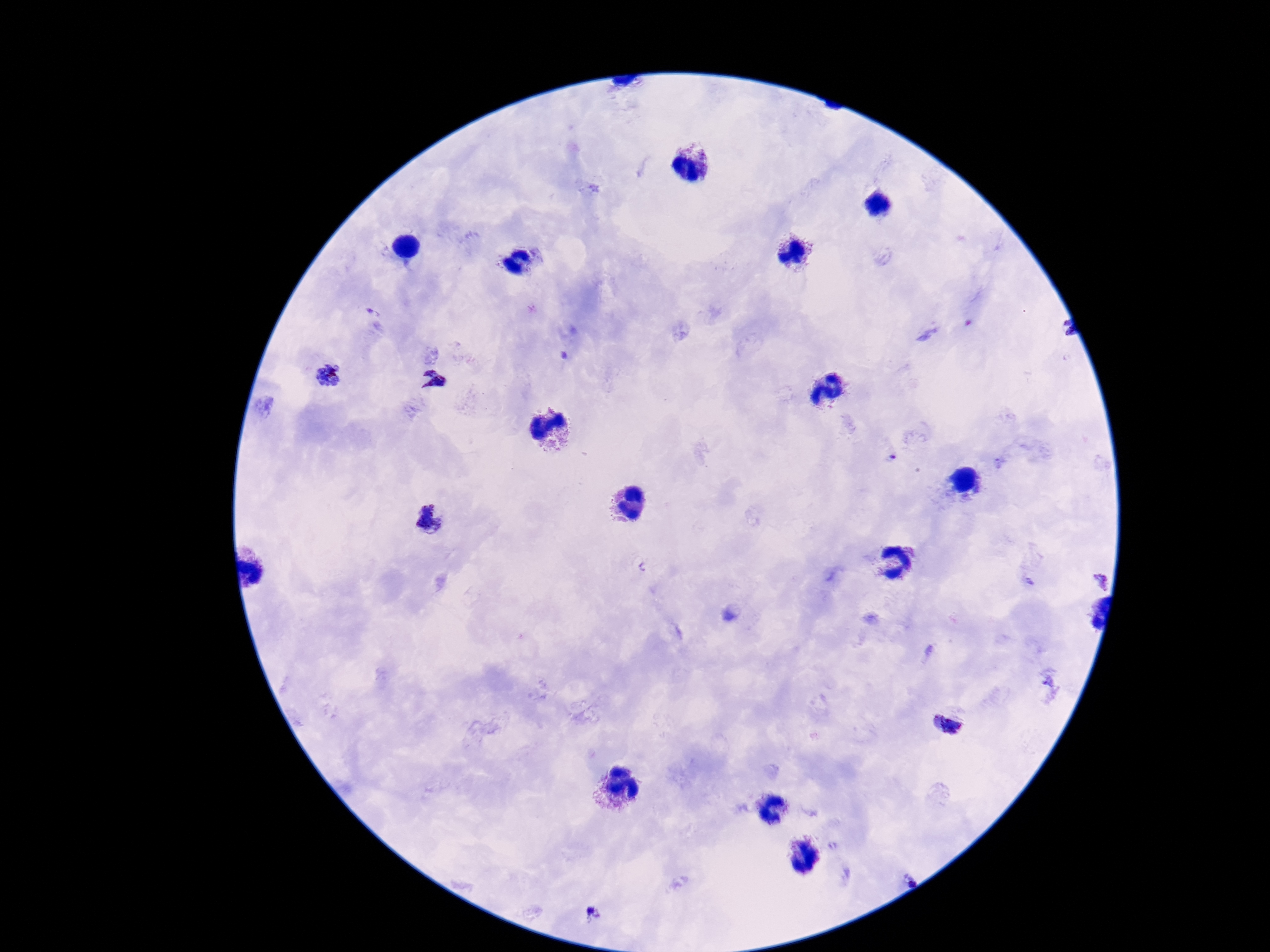

Approximate centers as (x, y) in pixels.
Summary:
  - Plasmodium parasite locations: (329, 375), (432, 377), (434, 523), (951, 722), (595, 916)
  - Field of view: single
  - Stain: Giemsa
  - Image size: 1270×952 pixels
  - Preparation: thick peripheral-blood smear
  - Patient malaria status: positive
  - Magnification: 100x
  - Capture: smartphone camera through the microscope eyepiece